Classify this cell by malaria status.
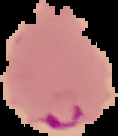

Parasitized.

The area outside the segmented cell region is set to black. Image is 118×136 pixels. From a thin blood smear.